Classify this cell by malaria status.
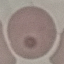
Uninfected.

Summary:
  - Capture: smartphone camera at the microscope eyepiece
  - Preparation: thin smear
  - Stain: Giemsa
  - Image type: cell patch, automatically extracted from a larger field of view and resized to 64 × 64 pixels